Identify the parasite.
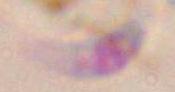

This is Toxoplasma gondii.

Summary:
  - Modality: micrograph
  - Magnification: 1000x